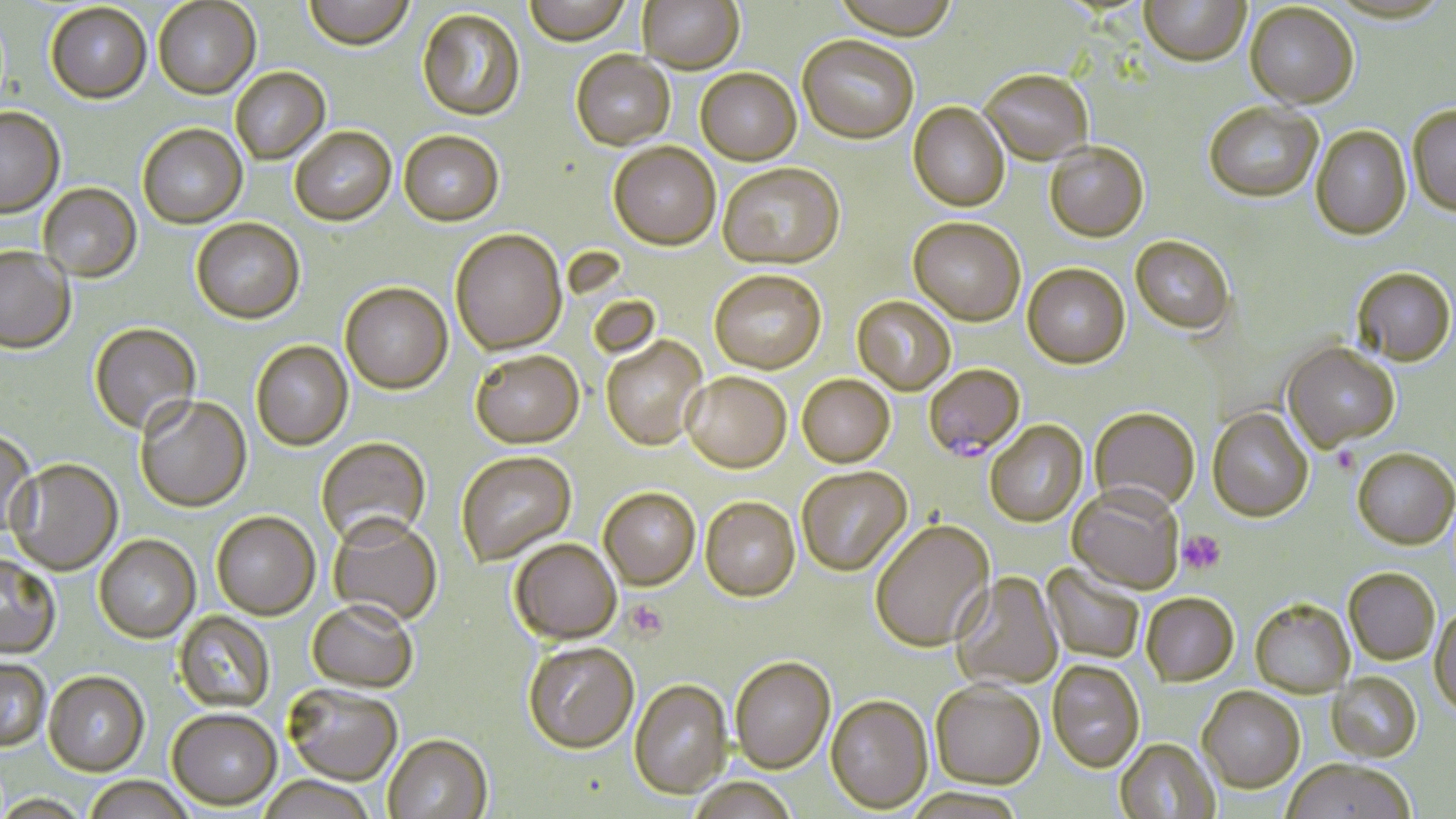

Approximate bounding boxes as [x1, y1, x2, y2] in pixels. Plasmodium falciparum-infected red blood cell locations: [924, 361, 1028, 464]. Uninfected red blood cell locations: [304, 0, 414, 52], [524, 0, 632, 48], [638, 0, 745, 75], [831, 0, 960, 43], [1140, 0, 1250, 70], [153, 1, 261, 101], [46, 4, 152, 105], [1245, 5, 1358, 111], [417, 9, 526, 123], [797, 37, 919, 146], [570, 52, 675, 152], [230, 68, 331, 165], [695, 70, 802, 167], [980, 72, 1093, 167], [1204, 103, 1323, 204], [908, 104, 1010, 214], [0, 107, 65, 218], [1408, 107, 1456, 218], [137, 124, 247, 229], [290, 127, 396, 226], [1310, 128, 1412, 242], [399, 131, 504, 228], [608, 143, 720, 253], [1044, 144, 1149, 244], [718, 165, 845, 271], [38, 182, 142, 282], [191, 218, 305, 324], [908, 218, 1025, 326], [450, 229, 567, 355], [1130, 237, 1235, 335], [0, 245, 76, 353], [1022, 264, 1130, 370], [709, 270, 827, 375], [1352, 270, 1456, 369], [340, 282, 453, 394], [852, 296, 956, 396], [89, 322, 201, 436], [601, 336, 708, 451], [251, 340, 353, 451], [1282, 343, 1399, 453], [470, 350, 584, 449], [681, 372, 791, 474], [797, 374, 895, 468], [135, 395, 252, 512], [1207, 407, 1314, 523], [1088, 408, 1200, 515], [985, 421, 1088, 527], [0, 430, 38, 538], [316, 437, 431, 547], [456, 450, 576, 565], [1352, 450, 1455, 551], [7, 458, 123, 575], [797, 466, 912, 576], [1067, 486, 1184, 594], [598, 487, 701, 590], [700, 497, 800, 602], [211, 510, 320, 619], [328, 513, 443, 627], [870, 520, 995, 653], [95, 534, 201, 642], [509, 537, 621, 644], [0, 554, 61, 658], [1043, 563, 1145, 664], [1343, 569, 1439, 666], [951, 572, 1063, 691], [1141, 593, 1239, 687], [307, 600, 418, 692], [1250, 600, 1355, 699], [1430, 604, 1456, 717], [173, 611, 276, 712], [522, 640, 639, 753], [730, 655, 836, 773], [0, 657, 50, 750], [1047, 660, 1145, 771], [44, 670, 149, 776], [1327, 672, 1422, 763], [628, 678, 732, 798], [930, 680, 1045, 789], [283, 682, 403, 785], [1197, 686, 1305, 795], [826, 694, 933, 813], [167, 707, 281, 810], [383, 733, 493, 819], [1115, 739, 1219, 819], [1282, 761, 1416, 819], [83, 776, 194, 819], [258, 776, 379, 819], [687, 777, 800, 819], [0, 794, 93, 818]. Platelet locations: [1178, 530, 1226, 574], [624, 600, 668, 642]. Slide-level diagnosis: Plasmodium falciparum. Captured at 1000x magnification. Image is 1456×819 pixels. May-Grünwald-Giemsa-stained preparation. Optical microscopy. Single field of view. Thin blood film.